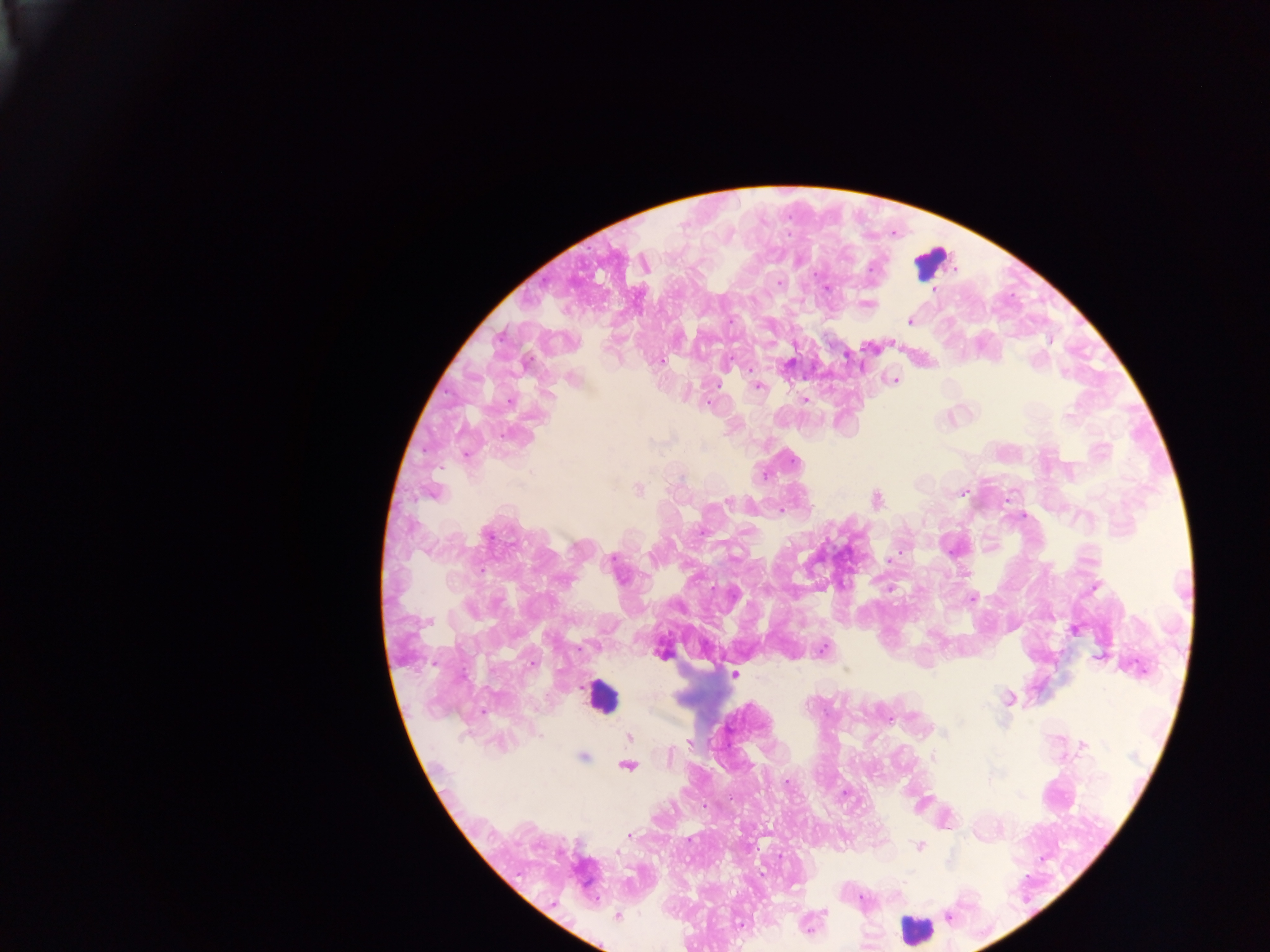
preparation = thick blood smear
country = Ghana
field of view = single
capture = mobile-phone photograph through a microscope
malaria parasite locations = approximate centers as x y in pixels: 871 267; 779 282; 826 289; 932 289; 868 303; 910 320; 661 360; 789 363; 894 380; 758 387; 804 399; 509 402; 1069 415; 795 461; 765 475; 638 488; 963 492; 433 493; 876 499; 727 501; 779 510; 701 532; 487 536; 612 559; 889 560; 966 572; 1094 588; 890 590; 973 598; 428 621; 1075 630; 822 650; 662 654; 1100 656; 734 674; 1009 699; 944 733; 629 738; 690 742; 1083 745; 670 756; 583 757; 933 757; 628 766; 787 781; 1019 796; 629 835; 919 846; 618 852; 861 899; 824 912; 617 917; 948 917; 740 924; 809 929
image size = 1270×952 pixels
leukocyte locations = approximate centers as x y in pixels: 932 261; 601 696; 916 930